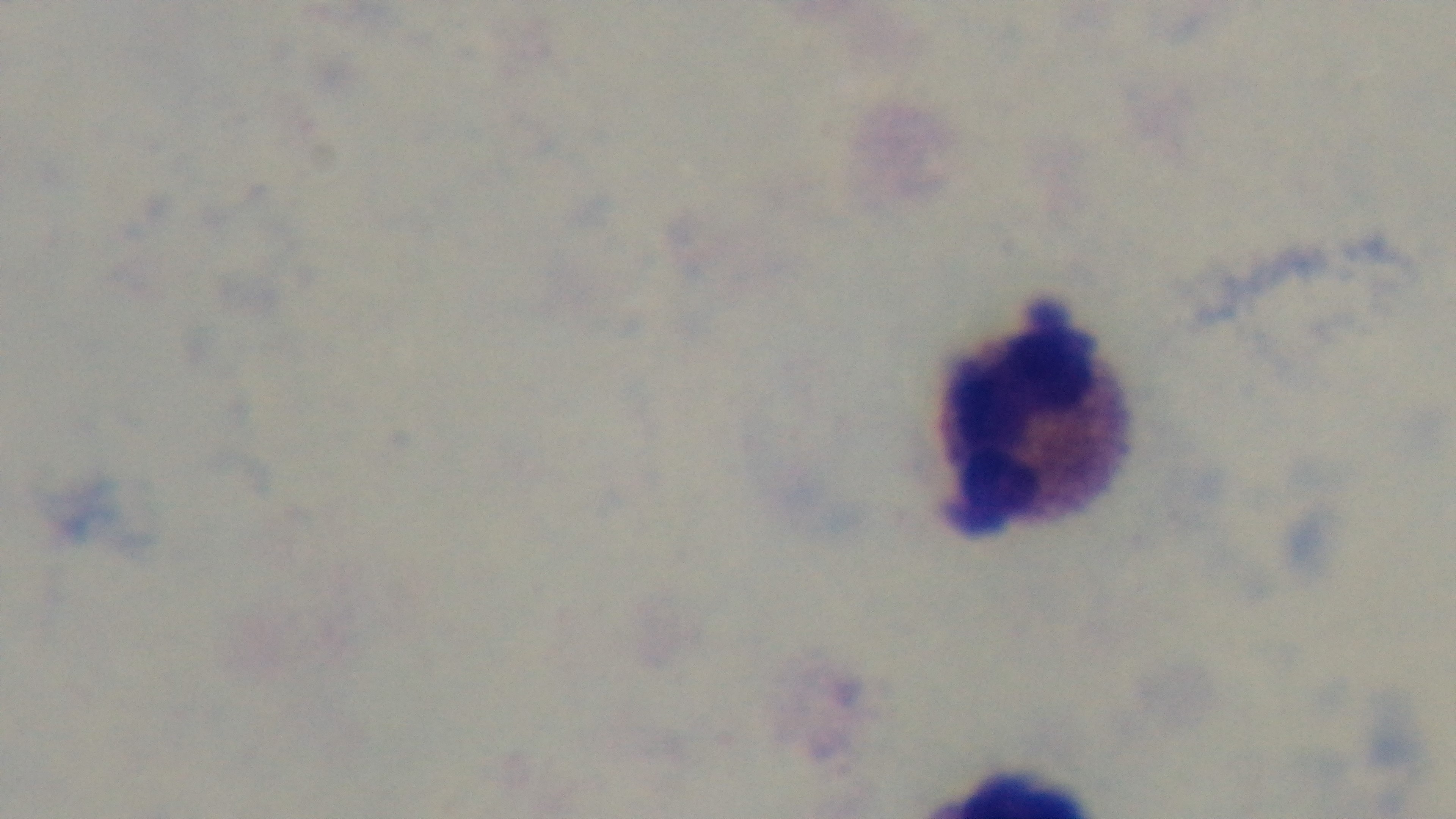

Captured with a mounted 4K digital camera. Malaria status: negative. Photomicrograph. One field from the slide. Giemsa-stained. Oil-immersion objective, 100x. Preparation: thick blood film.